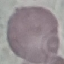

result = no malaria parasites detected
image type = cell patch, automatically extracted from a larger field of view and resized to 64 × 64 pixels
preparation = thin smear
stain = Giemsa
capture = smartphone camera at the microscope eyepiece